Mark where platelets are.
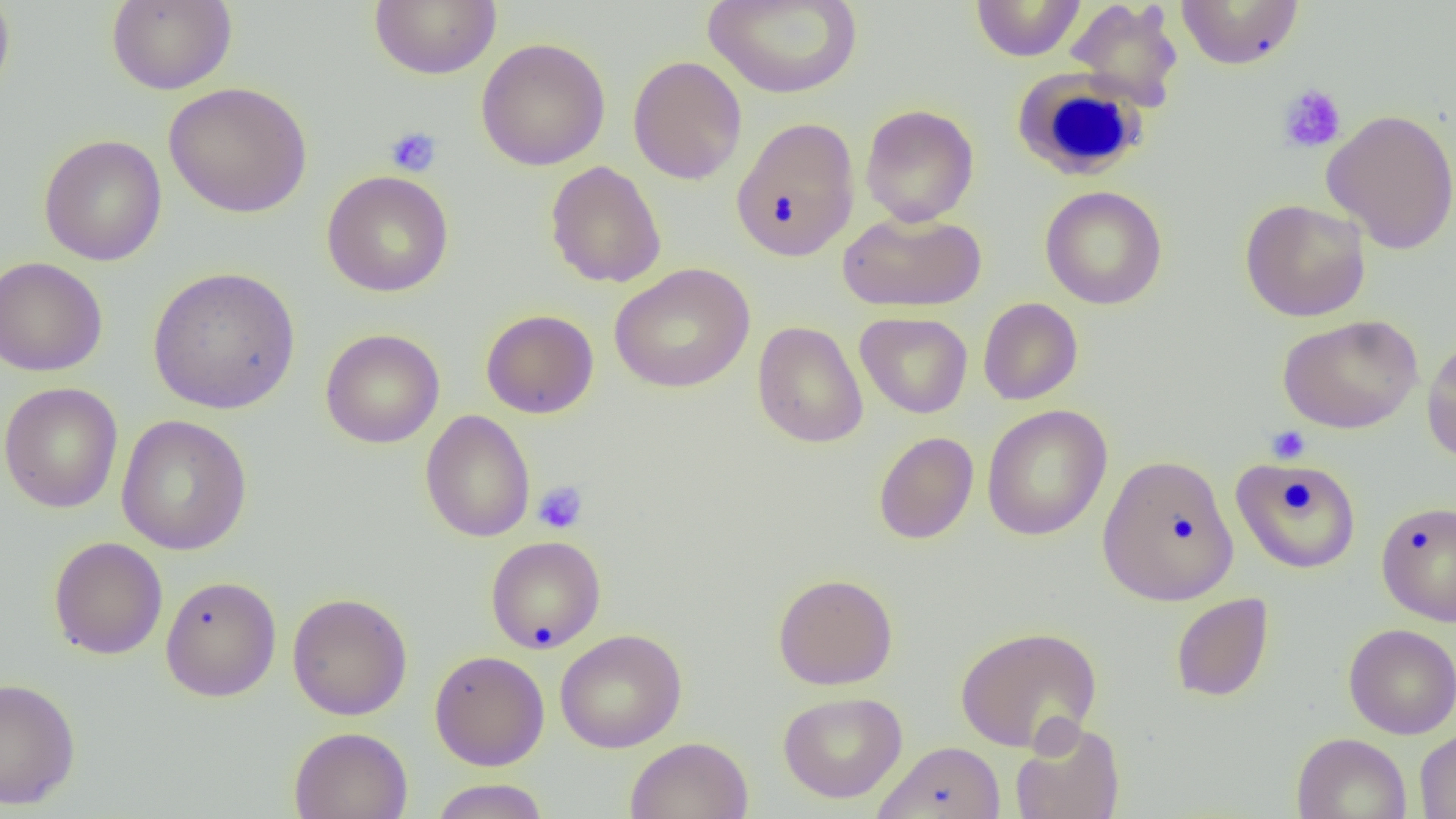
Approximate bounding boxes as (x1,y1)-(x2,y2) corner pairs in pixels.
Platelets: (1277,84)-(1347,154), (386,126)-(442,178), (1266,425)-(1311,464), (532,481)-(588,534).

{
  "slide_level_diagnosis": "no evidence of blood parasites",
  "white_blood_cell_locations": "approximate bounding boxes as (x1,y1)-(x2,y2) corner pairs in pixels: (1012,69)-(1149,181)",
  "preparation": "thin blood film",
  "modality": "light microscopy",
  "magnification": "1000x",
  "field_of_view": "single",
  "uninfected_red_blood_cell_locations": "approximate bounding boxes as (x1,y1)-(x2,y2) corner pairs in pixels: (106,0)-(237,95), (368,0)-(502,80), (704,0)-(863,99), (1065,0)-(1184,108), (1175,0)-(1305,70), (0,1)-(16,103), (970,1)-(1087,61), (476,37)-(611,171), (627,55)-(747,185), (163,81)-(313,218), (860,104)-(979,227), (1321,108)-(1456,255), (731,116)-(860,262), (38,134)-(167,266), (546,161)-(666,288), (321,170)-(454,297), (1040,185)-(1168,310), (1239,198)-(1371,322), (837,210)-(987,313), (0,257)-(108,377), (609,263)-(755,393), (147,266)-(301,415), (978,297)-(1083,405), (481,309)-(599,418), (856,312)-(973,418), (1277,314)-(1423,434), (752,321)-(868,448), (320,328)-(445,449), (1421,335)-(1456,464), (0,381)-(123,513), (981,405)-(1112,541), (420,410)-(535,542), (116,414)-(253,556), (873,431)-(979,545), (1097,454)-(1239,606), (1231,457)-(1360,574), (1375,500)-(1456,626), (485,535)-(605,653), (48,536)-(168,660), (773,572)-(898,690), (161,574)-(281,703), (287,592)-(413,721), (1170,593)-(1274,702), (1343,623)-(1456,739), (954,625)-(1103,752), (555,628)-(687,753), (429,650)-(550,770), (0,676)-(81,810), (778,691)-(907,803), (1010,718)-(1125,819), (288,726)-(413,819), (1415,727)-(1456,818), (1291,732)-(1412,819), (624,736)-(754,819), (872,741)-(1007,818), (429,779)-(550,818)",
  "image_size": "1456×819 pixels"
}